Identify the blood parasite species.
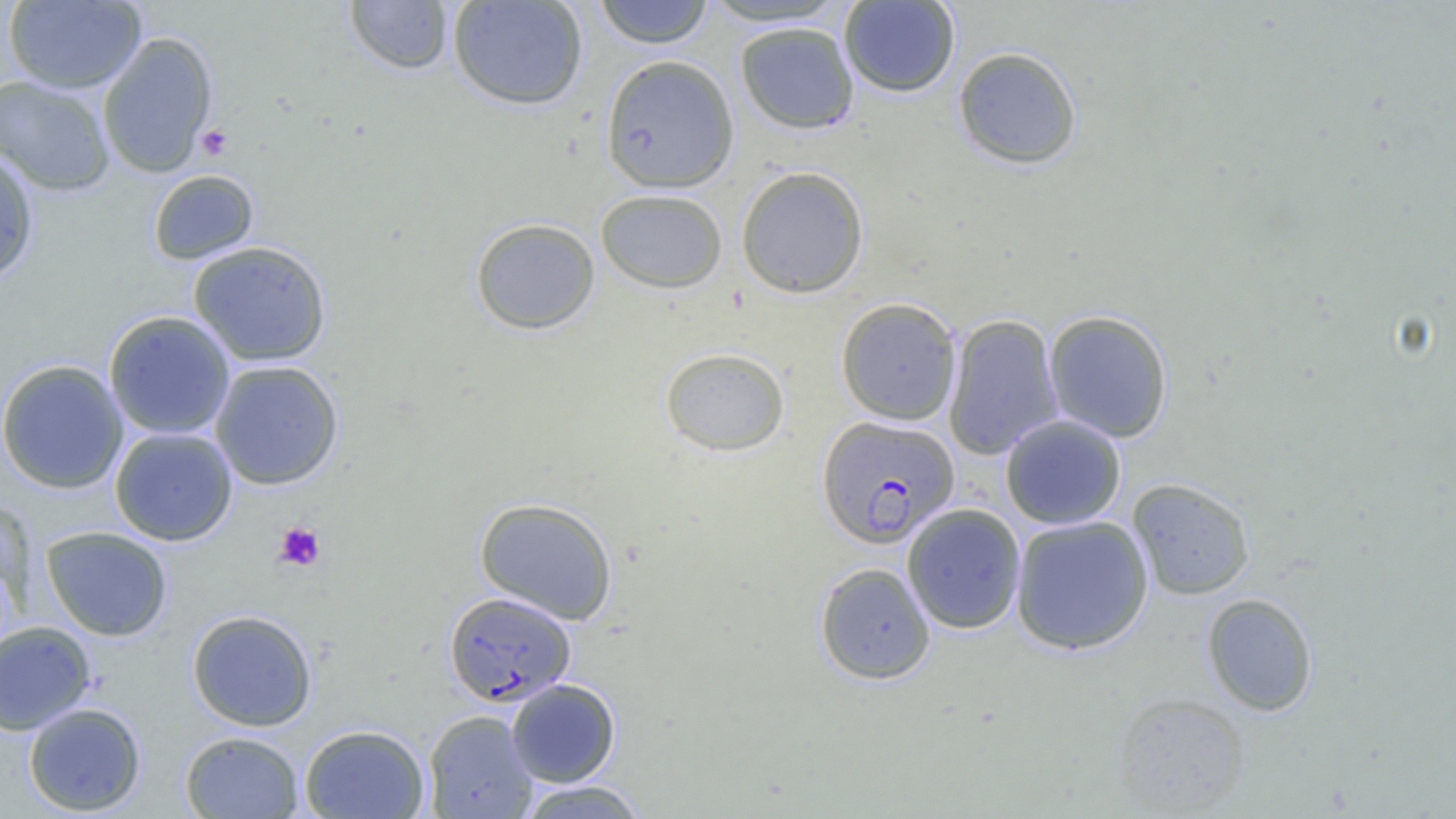

Plasmodium falciparum.

Approximate bounding boxes as (x1,y1)-(x2,y2) corner pairs in pixels. Uninfected red blood cell locations: (447,0)-(589,111), (594,0)-(714,49), (838,0)-(961,98), (3,1)-(147,94), (344,1)-(455,75), (697,1)-(852,28), (734,21)-(860,135), (98,31)-(217,178), (952,46)-(1083,170), (600,54)-(739,194), (1,74)-(115,196), (0,146)-(40,286), (736,166)-(870,298), (148,169)-(259,265), (596,188)-(728,293), (470,217)-(600,335), (188,240)-(332,367), (835,297)-(962,425), (103,310)-(236,440), (1043,310)-(1174,443), (943,313)-(1064,460), (659,346)-(790,457), (0,359)-(129,495), (209,360)-(344,491), (999,414)-(1127,530), (109,427)-(238,546), (1127,477)-(1255,600), (474,497)-(619,624), (901,503)-(1026,634), (1010,515)-(1154,655), (41,525)-(173,641), (814,562)-(936,685), (1201,592)-(1318,716), (187,609)-(318,731), (0,621)-(96,735), (506,678)-(621,787), (1112,692)-(1251,816), (23,702)-(147,816), (423,710)-(538,819), (299,724)-(430,819), (180,730)-(305,818), (516,780)-(650,819). Plasmodium falciparum-infected red blood cell locations: (816,415)-(959,548), (443,590)-(576,707). Platelet locations: (196,124)-(234,161), (273,521)-(326,572). 1000x magnification. Single field of view. Thin blood film. Light microscopy. Image is 1456×819 pixels.